Give the position of every Plasmodium parasite visible.
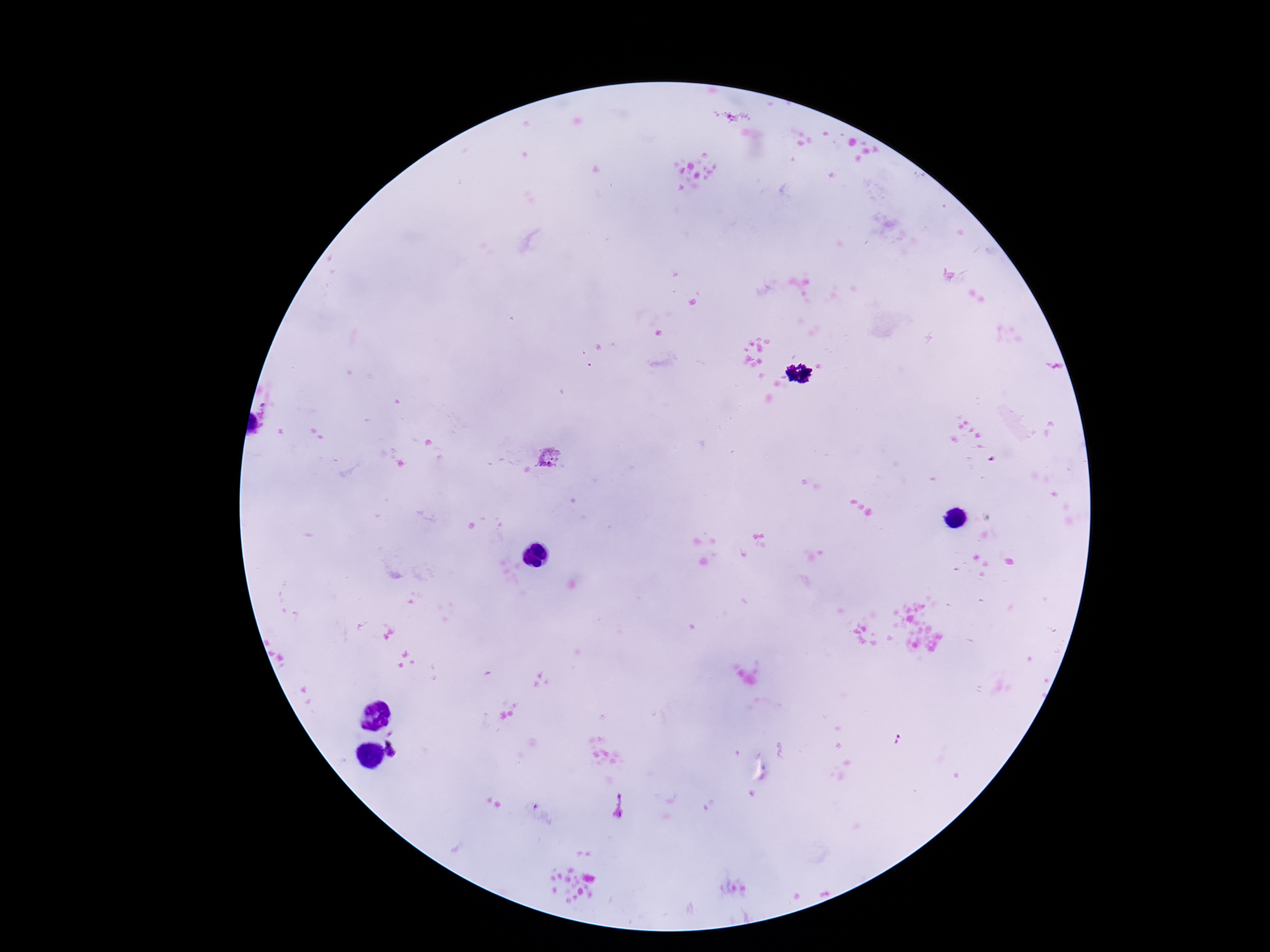

Approximate centers as (x, y) in pixels.
Plasmodium parasites: (549, 458), (396, 747).

capture = smartphone camera through the microscope eyepiece
preparation = thick peripheral-blood smear
patient malaria status = infected
stain = Giemsa
field of view = one from this slide
image size = 1270×952 pixels
magnification = 100x